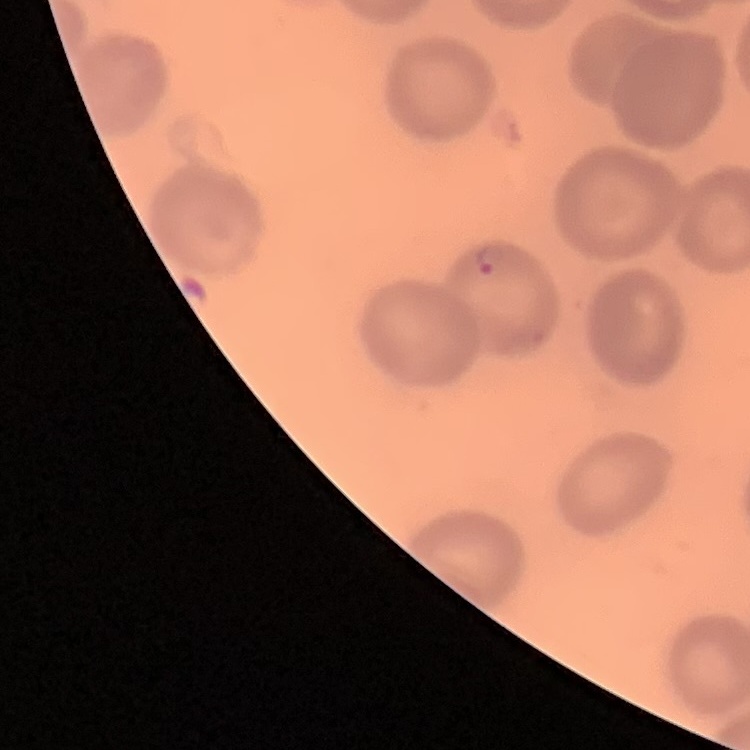

red blood cell morphology = no rouleaux formation
preparation = thin peripheral smear
stain = Field's or Giemsa
image type = one tile cut from a larger photomicrograph